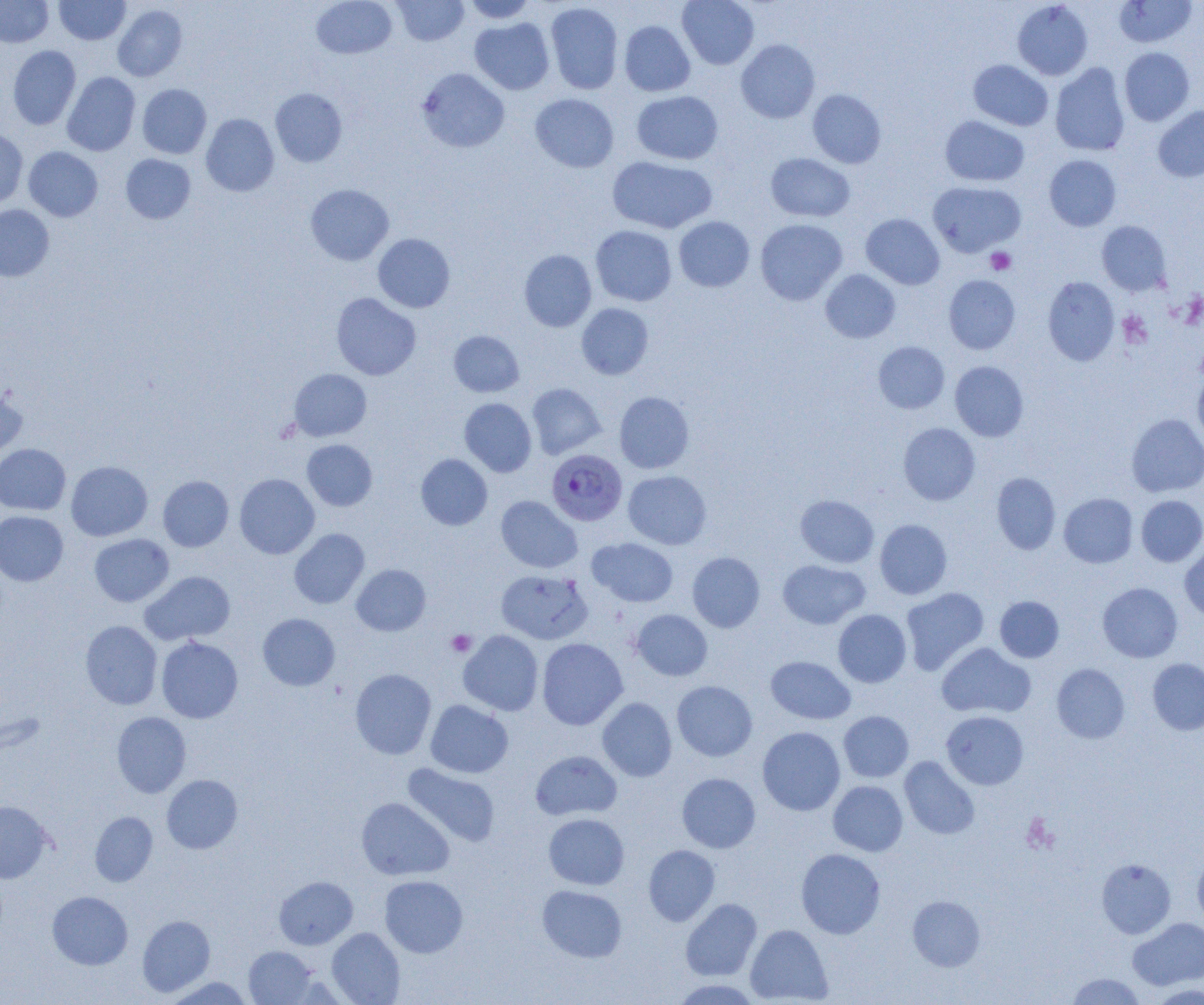

Approximate bounding boxes as (x1, y1, x2, y2) in pixels. Uninfected red blood cell locations: (0, 0, 53, 47), (54, 0, 130, 45), (311, 0, 397, 59), (392, 0, 469, 46), (462, 0, 538, 23), (677, 0, 759, 69), (1113, 0, 1198, 48), (1012, 1, 1093, 80), (545, 2, 623, 94), (113, 4, 188, 81), (470, 18, 555, 95), (619, 20, 695, 96), (736, 39, 820, 123), (8, 45, 81, 130), (1119, 47, 1194, 126), (968, 60, 1053, 131), (1050, 63, 1130, 156), (416, 68, 510, 153), (62, 72, 141, 156), (137, 84, 211, 159), (270, 88, 347, 167), (807, 89, 886, 168), (631, 90, 723, 165), (530, 93, 619, 173), (1153, 105, 1204, 182), (201, 113, 279, 196), (940, 115, 1029, 186), (0, 128, 28, 209), (24, 146, 103, 221), (766, 153, 855, 222), (121, 154, 196, 224), (1044, 154, 1121, 231), (607, 156, 716, 234), (928, 181, 1025, 257), (305, 184, 394, 265), (0, 204, 54, 281), (861, 213, 944, 289), (674, 216, 754, 292), (755, 219, 847, 305), (1097, 221, 1171, 296), (590, 225, 677, 306), (373, 233, 455, 312), (519, 250, 597, 332), (820, 269, 900, 343), (943, 275, 1020, 354), (1042, 276, 1120, 366), (331, 293, 421, 380), (576, 303, 653, 379), (448, 330, 524, 397), (873, 341, 949, 413), (950, 361, 1029, 441), (1193, 367, 1204, 450), (289, 369, 371, 441), (527, 383, 606, 459), (0, 387, 27, 459), (614, 391, 694, 474), (459, 398, 537, 477), (1126, 413, 1204, 497), (898, 422, 980, 505), (302, 439, 377, 511), (0, 444, 70, 514), (416, 453, 492, 530), (66, 460, 152, 541), (623, 470, 711, 549), (991, 472, 1061, 554), (234, 473, 319, 559), (158, 475, 233, 552), (1058, 493, 1138, 567), (795, 495, 878, 568), (1136, 495, 1204, 567), (496, 496, 582, 573), (0, 511, 69, 586), (874, 519, 952, 599), (289, 528, 369, 608), (89, 533, 174, 606), (587, 537, 678, 607), (1179, 542, 1204, 621), (687, 552, 765, 632), (778, 559, 869, 629), (351, 564, 431, 636), (496, 569, 593, 644), (141, 571, 235, 645), (1097, 582, 1183, 662), (901, 587, 989, 675), (995, 596, 1064, 663), (631, 609, 712, 680), (833, 609, 911, 687), (258, 613, 340, 690), (80, 620, 162, 709), (458, 630, 544, 716), (156, 637, 243, 723), (537, 638, 627, 729), (936, 642, 1035, 719), (766, 656, 855, 724), (1147, 658, 1204, 735), (1051, 663, 1130, 744), (350, 668, 436, 759), (672, 681, 757, 761), (597, 697, 677, 781), (425, 700, 513, 778), (112, 711, 191, 797), (838, 711, 914, 782), (941, 711, 1029, 790), (757, 726, 845, 815), (530, 750, 622, 820), (900, 756, 980, 839), (403, 763, 500, 847), (677, 772, 760, 853), (162, 774, 243, 854), (828, 780, 908, 856), (356, 797, 453, 880), (0, 801, 52, 883), (90, 811, 157, 886), (543, 813, 629, 890), (643, 845, 720, 926), (795, 848, 885, 939), (1192, 853, 1204, 928), (1097, 858, 1176, 939), (380, 875, 468, 958), (274, 876, 358, 949), (537, 885, 627, 962), (47, 891, 133, 970), (907, 895, 985, 971), (680, 898, 762, 981), (137, 915, 215, 996), (1128, 918, 1204, 990), (745, 924, 833, 1004), (326, 927, 405, 1005), (244, 946, 318, 1004), (1067, 973, 1146, 1004), (163, 976, 255, 1004), (669, 979, 763, 1004), (1148, 984, 1203, 1004). Plasmodium falciparum-infected red blood cell locations: (546, 449, 628, 526). Platelet locations: (986, 248, 1016, 274), (1118, 311, 1152, 348), (446, 629, 476, 656), (1023, 815, 1058, 852). Slide-level diagnosis: Plasmodium falciparum. Thin blood film. Optical microscopy. Captured at 1000x magnification. One field of a larger specimen. Image is 1204×1005 pixels.